Draw a bounding box around every Plasmodium parasite.
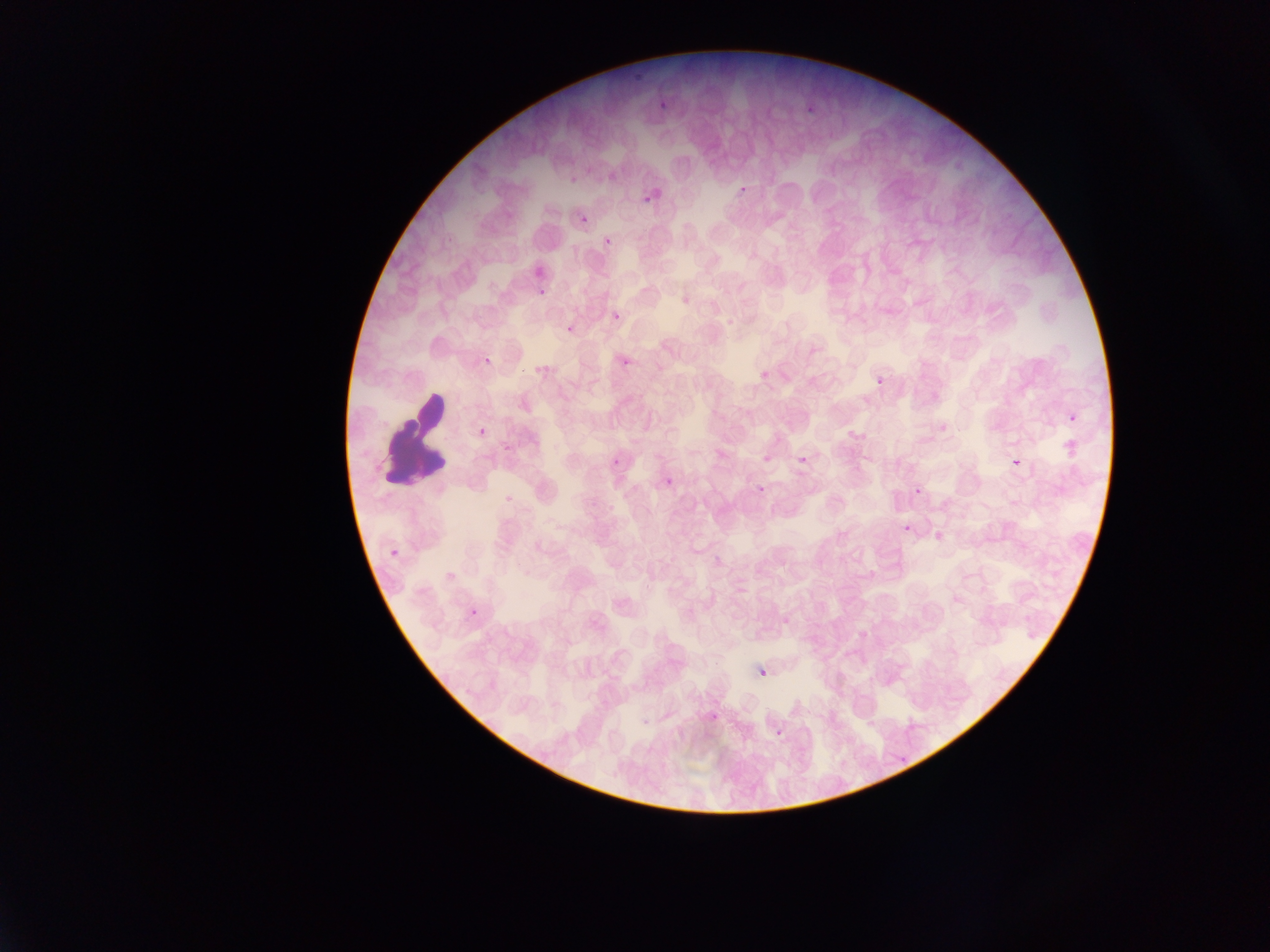

Approximate bounding boxes as (left, top, right, bottom) in pixels.
Plasmodium parasites: (628, 69, 645, 94), (653, 95, 673, 112), (805, 103, 818, 117), (734, 179, 749, 199), (639, 188, 661, 210), (578, 212, 590, 226), (601, 234, 616, 250), (534, 281, 552, 304), (610, 305, 625, 321), (611, 311, 623, 323), (562, 321, 579, 338), (470, 348, 505, 380), (619, 354, 634, 370), (873, 373, 890, 393), (1066, 409, 1083, 429), (475, 423, 492, 443), (1061, 436, 1082, 461), (794, 451, 813, 471), (1009, 453, 1027, 477), (610, 454, 628, 473), (663, 476, 676, 490), (753, 482, 770, 499), (911, 486, 926, 504), (899, 520, 918, 540), (386, 543, 406, 566), (464, 604, 484, 626), (758, 667, 770, 680), (769, 723, 786, 738), (892, 747, 916, 766).

Leukocyte locations: (387, 387, 455, 495). Photographed through a microscope with a mobile-phone camera. Single field of view. Thin blood smear. Sample from Ghana. Image is 1270×952 pixels.